State which cell type is depicted.
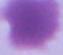
An erythrocyte.

{
  "modality": "photomicrograph",
  "magnification": "1000x"
}